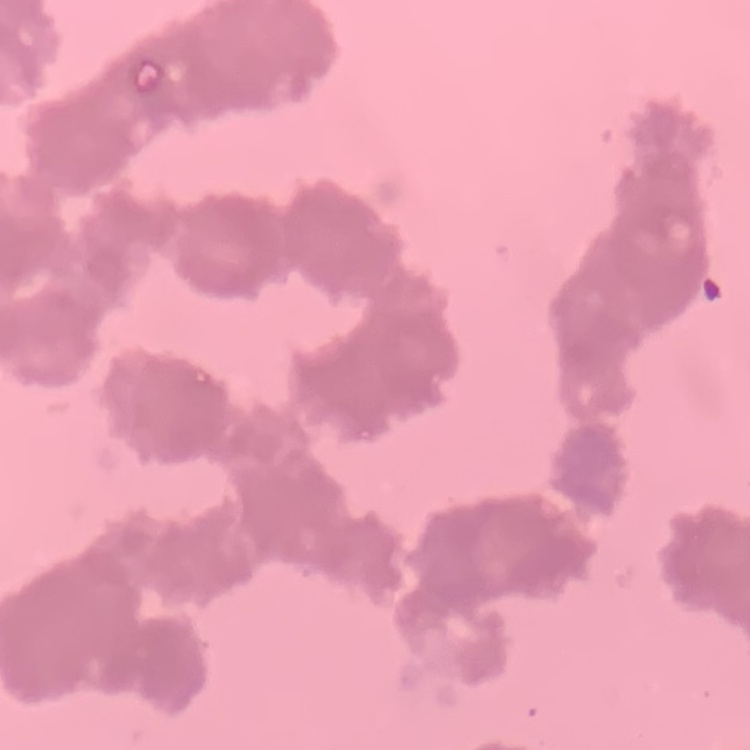
Summary:
  - Red blood cell morphology: rouleaux formation
  - Stain: Field's or Giemsa
  - Image type: one tile cut from a larger photomicrograph
  - Preparation: thin blood smear